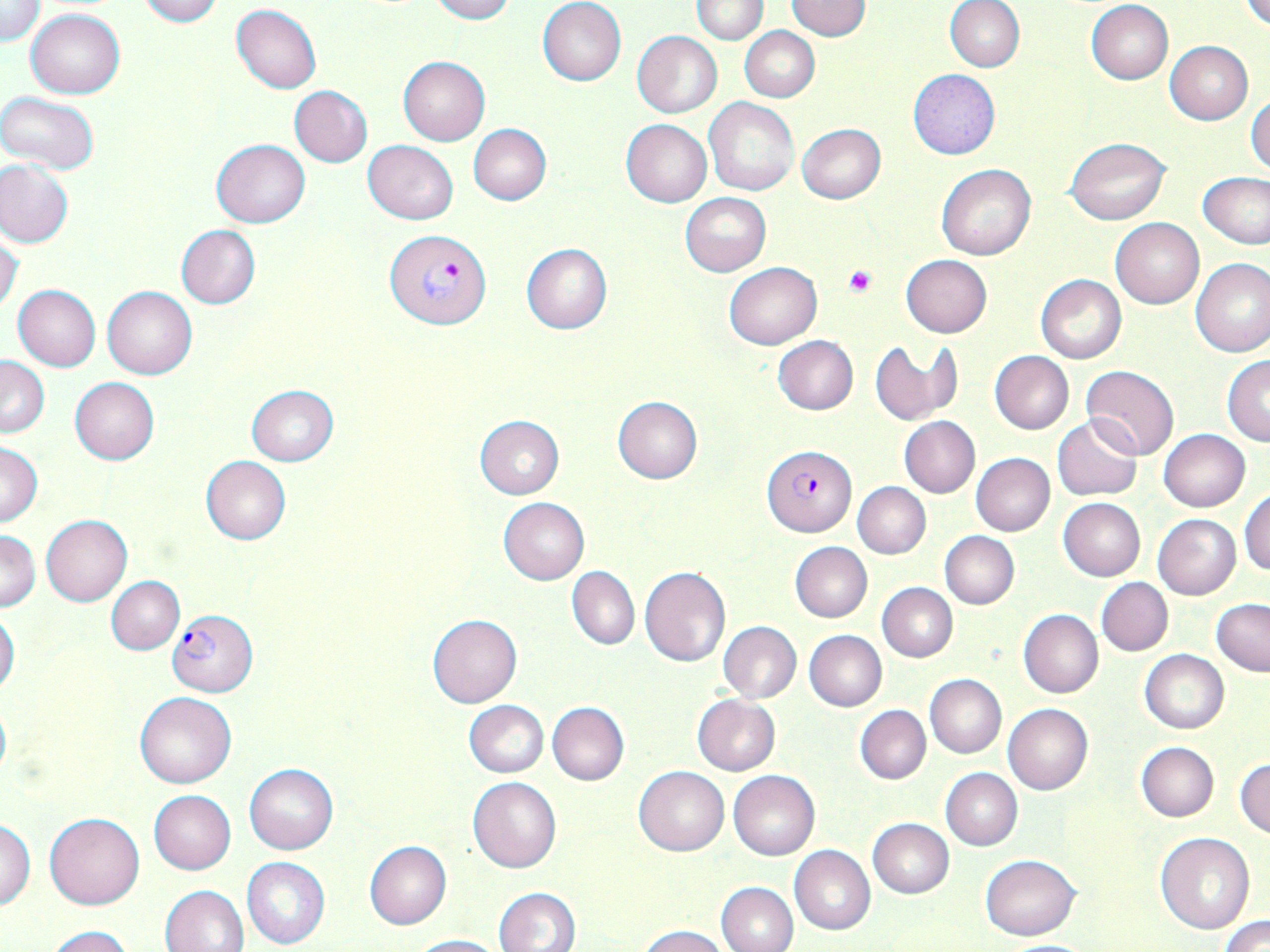

Summary:
  - Coordinate format: approximate bounding boxes as (x1,y1)-(x2,y2) corner pairs in pixels
  - Platelet locations: (843,265)-(878,298)
  - Plasmodium falciparum-infected red blood cell locations: (385,229)-(489,328), (764,445)-(856,536), (168,609)-(258,696)
  - Uninfected red blood cell locations: (137,0)-(221,26), (428,0)-(514,22), (692,0)-(768,44), (945,0)-(1025,72), (1242,0)-(1270,29), (1,1)-(44,45), (785,1)-(872,40), (1086,1)-(1173,84), (537,2)-(627,85), (231,4)-(321,93), (26,8)-(125,99), (740,26)-(820,101), (632,30)-(721,118), (1165,42)-(1252,124), (398,56)-(489,145), (908,69)-(1000,160), (290,86)-(372,167), (0,91)-(101,174), (1246,91)-(1270,176), (704,97)-(799,195), (621,118)-(712,207), (796,122)-(886,203), (469,123)-(551,205), (1064,137)-(1172,225), (212,139)-(309,227), (363,140)-(457,224), (0,158)-(74,247), (937,164)-(1035,260), (1198,172)-(1270,249), (680,193)-(770,277), (1110,217)-(1204,309), (176,224)-(260,309), (0,233)-(24,316), (521,244)-(613,334), (901,254)-(992,337), (1190,258)-(1270,357), (725,262)-(821,348), (1035,275)-(1125,364), (13,284)-(101,371), (101,285)-(197,379), (771,335)-(858,415), (870,340)-(950,425), (989,351)-(1074,435), (1,356)-(49,436), (1222,356)-(1270,446), (1081,365)-(1179,459), (69,377)-(160,464), (246,385)-(338,465), (612,396)-(703,483), (1053,415)-(1142,501), (475,416)-(565,498), (900,416)-(980,498), (1157,429)-(1250,511), (1,443)-(42,526), (971,454)-(1054,536), (200,456)-(290,545), (853,482)-(930,558), (1240,488)-(1269,575), (498,497)-(589,584), (1057,498)-(1145,581), (1153,513)-(1241,598), (41,515)-(131,605), (0,530)-(41,611), (940,531)-(1019,608), (790,542)-(872,622), (639,565)-(731,667), (567,566)-(639,649), (107,576)-(185,654), (1096,577)-(1173,656), (877,583)-(957,662), (1212,598)-(1270,675), (0,610)-(20,696), (1018,610)-(1102,698), (427,615)-(522,708), (718,621)-(802,703), (804,630)-(886,711), (1140,650)-(1228,733), (925,674)-(1006,758), (135,691)-(236,789), (692,694)-(780,775), (0,696)-(11,786), (464,700)-(549,778), (547,702)-(629,785), (1004,704)-(1093,795), (855,705)-(931,783), (1137,742)-(1218,820), (1234,758)-(1270,838), (243,764)-(337,854), (634,766)-(729,855), (941,768)-(1022,850), (729,770)-(819,860), (468,776)-(562,874), (148,790)-(236,874), (44,810)-(145,909), (0,817)-(35,910), (867,818)-(954,897), (1154,834)-(1254,934), (365,841)-(451,929), (790,845)-(875,936), (980,854)-(1082,940), (240,856)-(331,948), (715,881)-(797,952), (161,884)-(249,952), (494,887)-(581,952), (1220,914)-(1270,952), (47,926)-(133,952), (638,926)-(732,952), (409,934)-(505,952)
  - Slide-level diagnosis: Plasmodium falciparum
  - Preparation: thin blood film
  - Stain: May-Grünwald-Giemsa
  - Modality: optical microscopy
  - Image size: 1270×952 pixels
  - Magnification: 1000x
  - Field of view: single